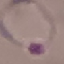
malaria status = parasitized
stain = Giemsa
capture = smartphone camera at the microscope eyepiece
preparation = thin blood film
image type = automatically extracted cell patch, resized to 64 × 64 pixels